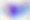

identification = Toxoplasma gondii
magnification = 400x
modality = micrograph